Locate and identify every blood parasite.
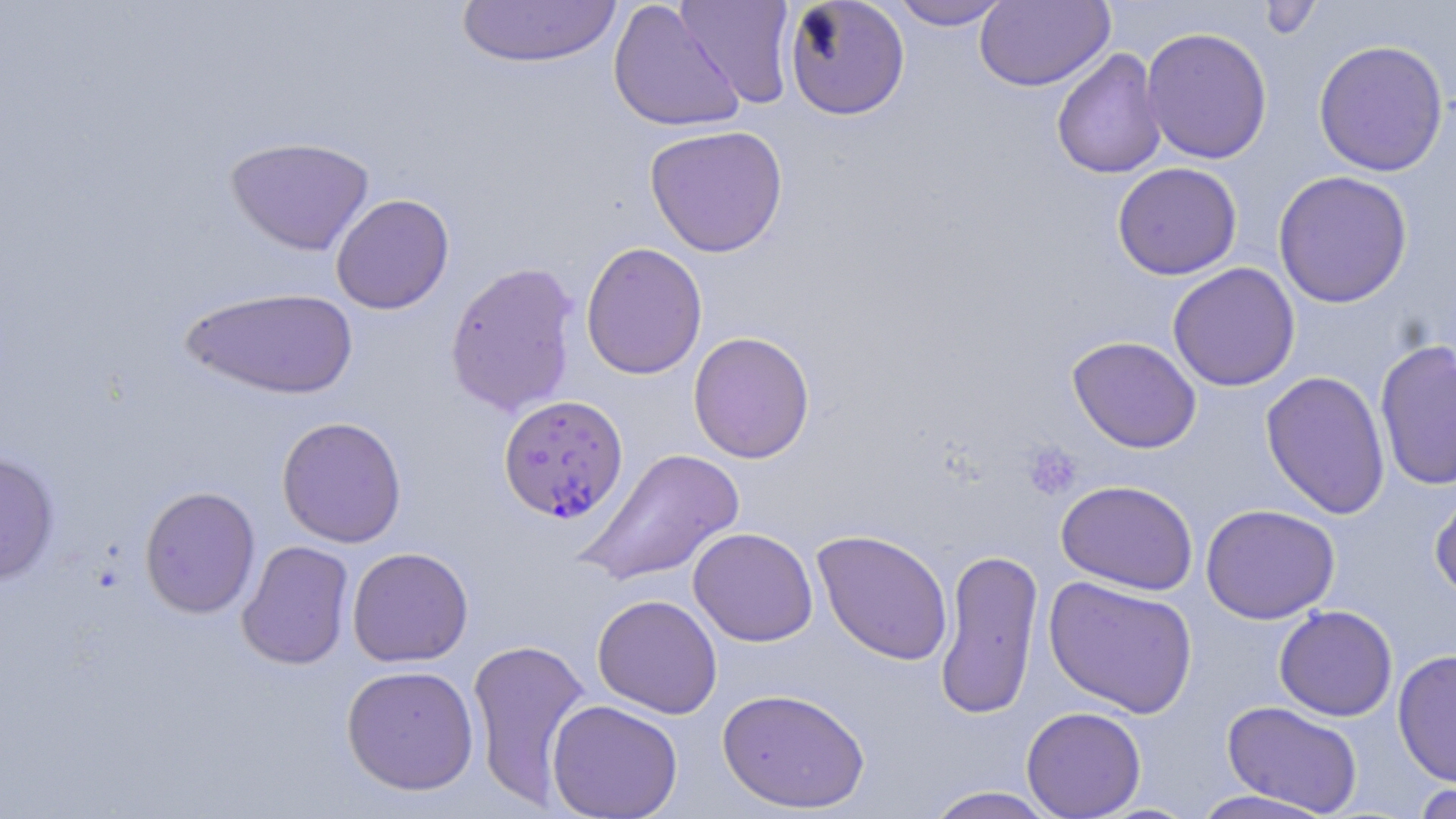

Approximate bounding boxes as [x1, y1, x2, y2] in pixels.
Plasmodium falciparum-infected red blood cells: [498, 394, 628, 523].
No Plasmodium ovale, Plasmodium malariae, Plasmodium vivax, Babesia divergens, or Trypanosoma brucei observed.

Platelet locations: [1023, 442, 1082, 501]. Uninfected red blood cell locations: [456, 0, 623, 68], [607, 0, 745, 134], [674, 0, 797, 108], [783, 0, 910, 120], [885, 0, 1012, 30], [1257, 0, 1324, 41], [975, 1, 1114, 91], [1141, 26, 1272, 164], [1312, 38, 1449, 177], [1051, 47, 1168, 179], [644, 125, 789, 257], [225, 135, 374, 256], [1112, 162, 1242, 280], [1273, 170, 1413, 308], [330, 193, 454, 314], [580, 241, 708, 380], [444, 260, 580, 417], [1168, 263, 1300, 391], [180, 286, 360, 400], [688, 331, 815, 463], [1067, 335, 1202, 453], [1374, 338, 1456, 492], [1260, 370, 1390, 519], [276, 416, 407, 548], [575, 448, 746, 588], [0, 452, 60, 585], [1055, 480, 1198, 595], [1430, 483, 1456, 602], [139, 485, 261, 619], [1200, 504, 1340, 624], [688, 527, 818, 647], [812, 529, 953, 666], [236, 540, 355, 670], [935, 546, 1043, 720], [347, 547, 474, 667], [1043, 576, 1199, 719], [592, 594, 723, 719], [1274, 605, 1398, 721], [466, 637, 593, 809], [1392, 649, 1456, 788], [341, 664, 479, 795], [717, 687, 870, 812], [546, 699, 684, 819], [1222, 701, 1363, 815], [1021, 706, 1147, 818], [1410, 782, 1456, 819], [923, 786, 1060, 819], [1188, 789, 1337, 819]. Slide-level diagnosis: Plasmodium falciparum. May-Grünwald-Giemsa-stained preparation. Thin blood film. 1000x magnification. Single field of view. Optical microscopy. Image is 1456×819 pixels.